Describe the morphology of the red blood cells.
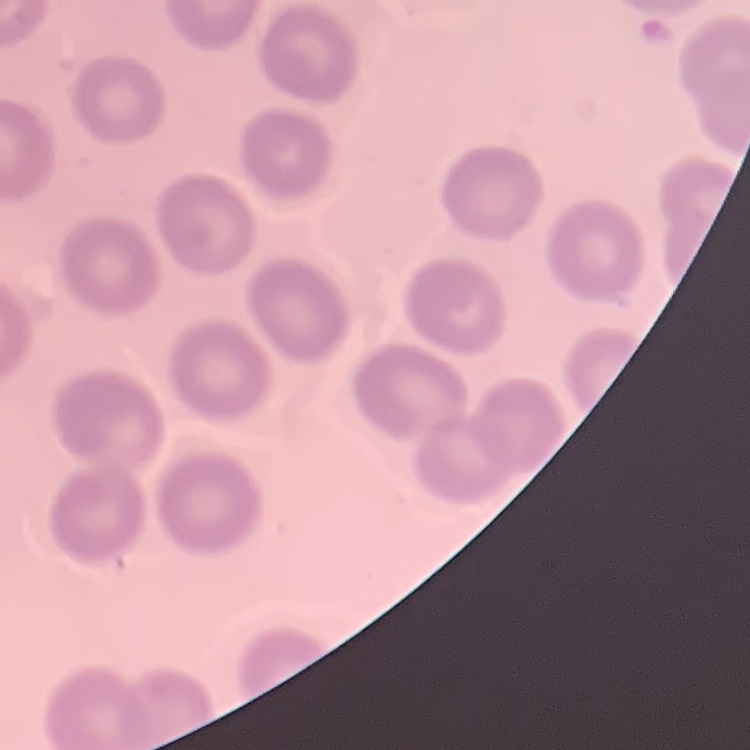

They show no rouleaux formation.

Summary:
  - Image type: square crop of a larger photomicrograph
  - Preparation: thin peripheral smear
  - Stain: Field's or Giemsa